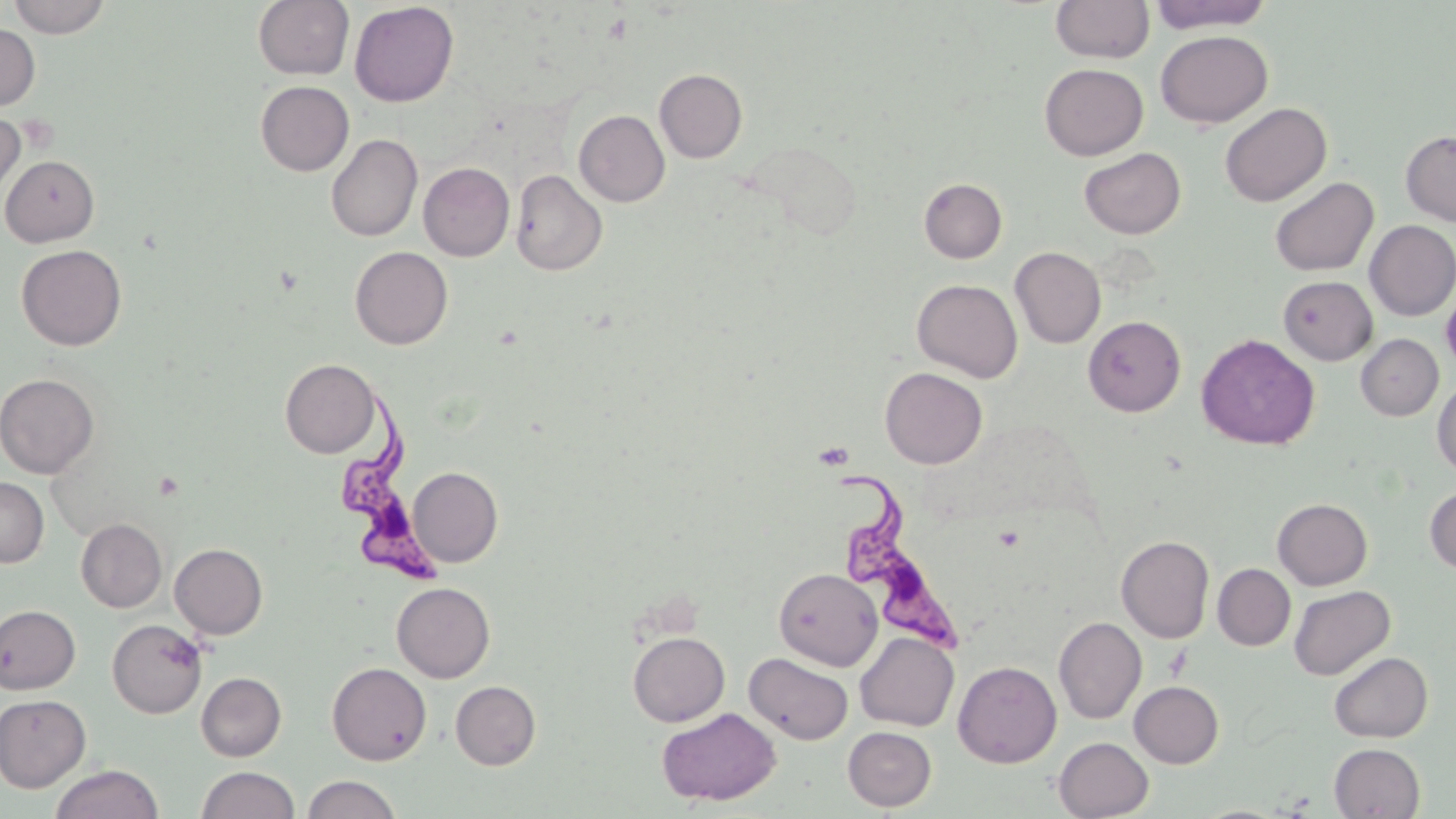
Summary:
  - Coordinate format: approximate bounding boxes as (x1, y1, x2, y2) in pixels
  - Trypanosoma brucei locations: (340, 392, 446, 586), (826, 469, 961, 651)
  - Uninfected red blood cell locations: (8, 0, 111, 37), (253, 0, 354, 80), (1051, 0, 1154, 63), (1148, 0, 1275, 33), (349, 1, 459, 107), (0, 24, 40, 111), (1155, 30, 1274, 128), (1039, 63, 1148, 160), (654, 68, 747, 163), (255, 81, 354, 176), (1220, 102, 1331, 206), (574, 110, 670, 207), (0, 114, 25, 202), (1400, 129, 1456, 226), (326, 134, 422, 241), (746, 140, 862, 240), (1079, 147, 1186, 239), (1, 154, 100, 247), (418, 162, 515, 261), (510, 169, 607, 276), (1269, 176, 1379, 276), (919, 178, 1007, 263), (1364, 220, 1456, 321), (16, 244, 127, 350), (350, 246, 453, 349), (1010, 247, 1106, 348), (1278, 275, 1377, 364), (912, 279, 1022, 382), (1083, 315, 1186, 416), (1196, 333, 1321, 450), (1356, 334, 1443, 420), (280, 359, 380, 458), (880, 367, 988, 468), (0, 373, 99, 478), (1432, 378, 1456, 477), (408, 467, 503, 567), (0, 477, 49, 567), (1425, 485, 1456, 574), (1272, 498, 1372, 590), (75, 518, 166, 612), (1116, 535, 1215, 643), (169, 543, 267, 638), (1212, 564, 1296, 650), (774, 567, 882, 671), (391, 582, 495, 683), (1289, 585, 1395, 680), (0, 604, 80, 694), (1053, 616, 1146, 724), (107, 619, 207, 718), (627, 631, 729, 726), (855, 632, 959, 731), (743, 650, 853, 746), (1328, 651, 1433, 742), (953, 661, 1061, 768), (327, 662, 431, 765), (196, 672, 286, 761), (450, 680, 541, 769), (1129, 680, 1224, 768), (0, 694, 91, 791), (657, 707, 781, 804), (843, 726, 936, 811), (1054, 736, 1153, 819), (1329, 743, 1426, 818), (49, 764, 164, 819), (196, 766, 299, 819), (302, 774, 402, 819)
  - Slide-level diagnosis: Trypanosoma brucei
  - Preparation: thin blood smear
  - Magnification: 1000x
  - Stain: May-Grünwald-Giemsa
  - Field of view: one of a larger specimen
  - Modality: optical microscopy
  - Image size: 1456×819 pixels